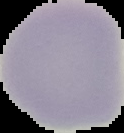 The area outside the segmented cell region is set to black. From a thin blood smear. Result: negative for malaria parasites. Image is 124×133 pixels.